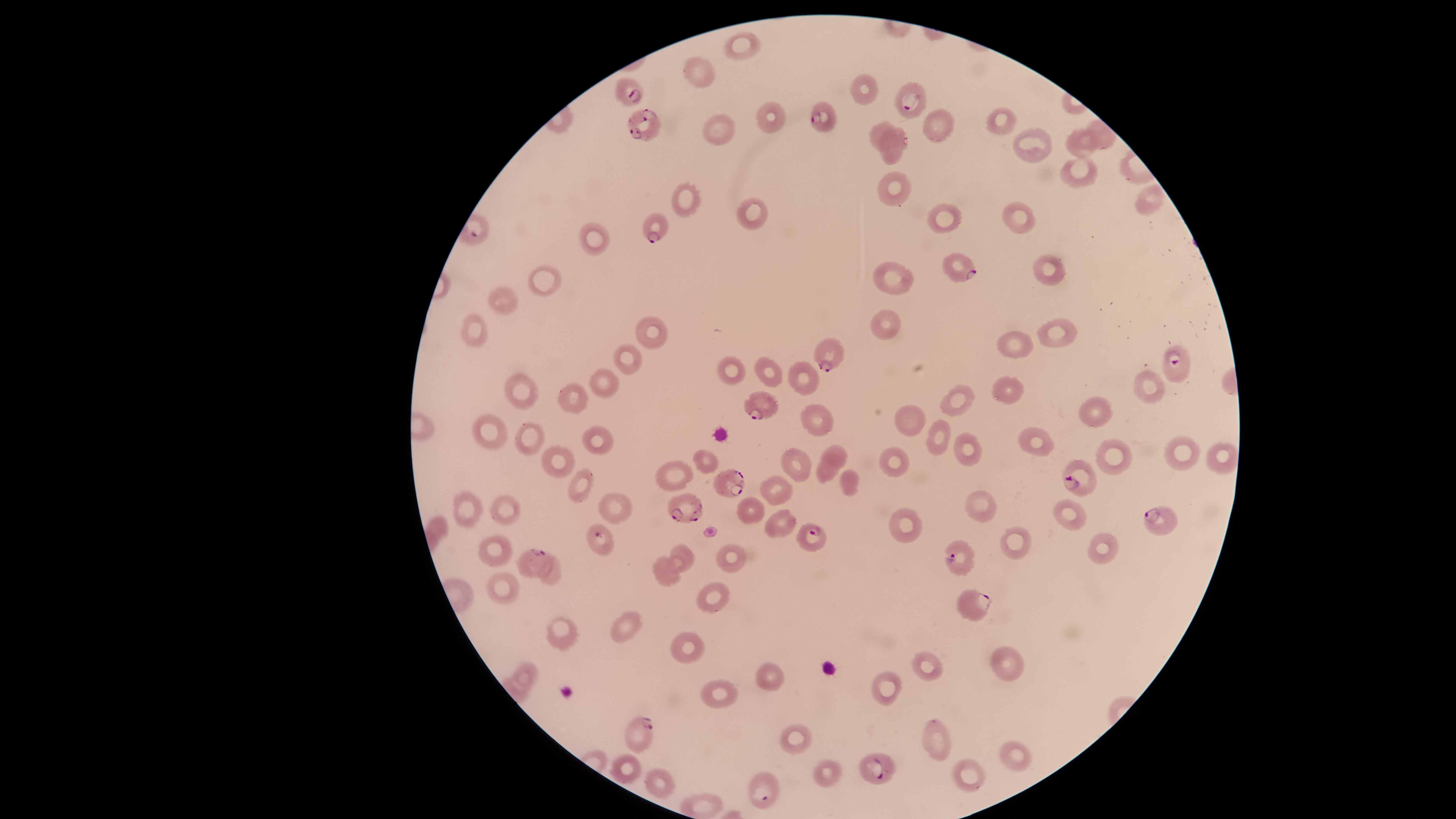

presence = malaria parasites detected
uninfected red blood cells = approximate marker points as [x, y] in pixels: [740, 40], [701, 72], [869, 88], [768, 112], [999, 120], [936, 126], [877, 129], [722, 131], [1101, 133], [1083, 144], [1031, 146], [891, 151], [1079, 172], [896, 189], [1144, 200], [691, 203], [752, 212], [943, 218], [1020, 218], [591, 235], [1046, 265], [552, 274], [898, 275], [505, 301], [885, 323], [471, 328], [656, 331], [1053, 332], [1017, 343], [625, 356], [731, 371], [770, 374], [806, 375], [604, 381], [1148, 384], [1015, 386], [516, 390], [575, 396], [963, 397], [1099, 409], [820, 415], [912, 418], [488, 431], [938, 434], [532, 439], [599, 440], [1037, 442], [1175, 450], [834, 451], [970, 453], [1111, 453], [1222, 456], [558, 457], [707, 460], [796, 461], [894, 461], [675, 473], [825, 474], [584, 476], [777, 488], [465, 505], [611, 505], [506, 507], [982, 510], [752, 511], [1074, 513], [775, 521], [905, 531], [1018, 545], [494, 546], [1104, 548], [682, 553], [728, 558], [552, 571], [664, 573], [502, 587], [708, 598], [561, 630], [630, 630], [684, 648], [1006, 661], [923, 663], [525, 675], [771, 676], [883, 691], [716, 697], [792, 731], [932, 740], [1007, 757], [629, 769], [829, 772], [661, 777], [967, 777], [701, 805]
preparation = thin blood film
image size = 1456×819 pixels
field of view = single
species = Plasmodium falciparum
capture = smartphone photograph through the microscope eyepiece
stain = Giemsa
visible region = circular
parasitized red blood cells = approximate marker points as [x, y] in pixels: [632, 90], [913, 95], [823, 117], [643, 120], [656, 226], [959, 267], [826, 351], [1171, 363], [762, 404], [1086, 477], [732, 481], [689, 506], [1155, 514], [811, 535], [595, 539], [959, 555], [529, 559], [975, 604], [640, 734], [885, 768], [764, 789]